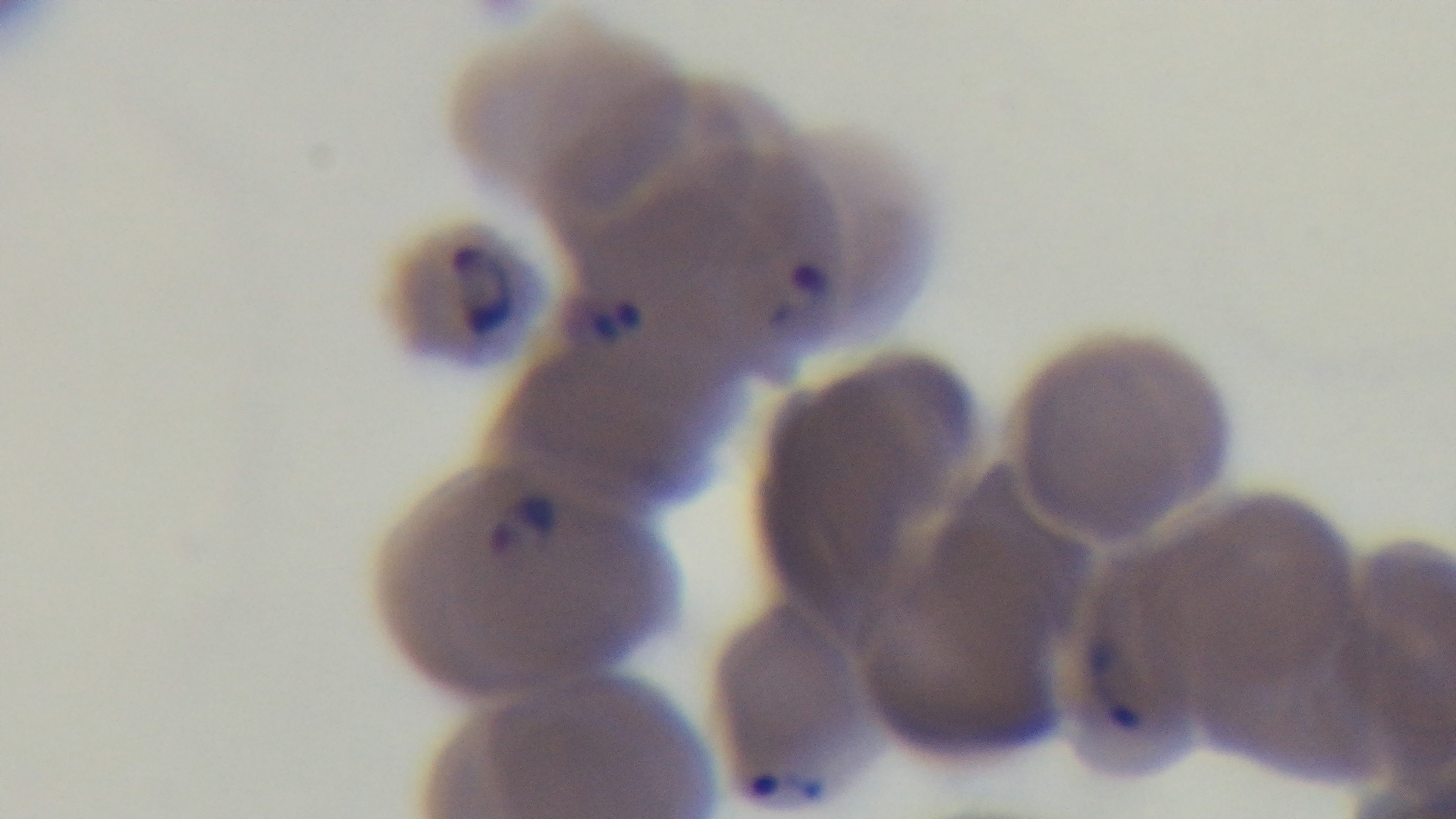
Summary:
  - Malaria status: infected
  - Preparation: thin
  - Modality: light microscopy
  - Stain: Giemsa
  - Capture: mounted 4K digital camera
  - Objective: 100x oil immersion
  - Field of view: one from the slide